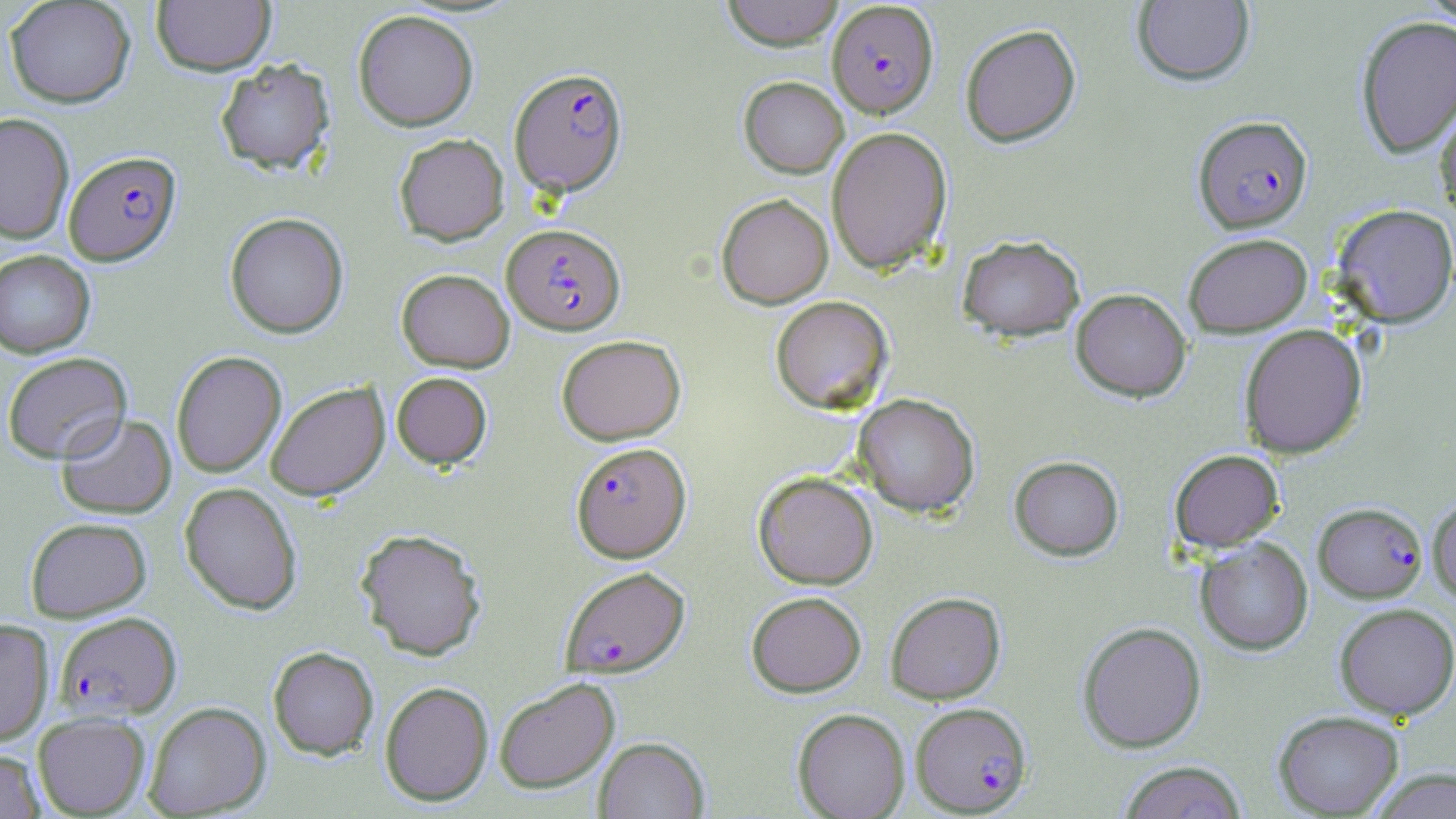

Summary:
  - Coordinate format: approximate bounding boxes as (x1, y1, x2, y2) in pixels
  - Uninfected red blood cell locations: (4, 0, 136, 108), (721, 0, 845, 50), (1418, 0, 1456, 27), (152, 1, 275, 75), (1132, 1, 1255, 86), (353, 9, 479, 131), (1354, 15, 1456, 158), (960, 23, 1081, 147), (215, 58, 335, 175), (738, 76, 849, 178), (1436, 96, 1456, 220), (0, 111, 74, 244), (826, 126, 952, 274), (394, 133, 509, 245), (716, 193, 833, 309), (1332, 203, 1456, 327), (224, 212, 349, 338), (1183, 232, 1313, 338), (957, 234, 1085, 341), (0, 250, 95, 358), (396, 268, 515, 372), (1071, 288, 1192, 402), (770, 295, 893, 413), (1239, 324, 1367, 459), (556, 334, 686, 445), (2, 351, 132, 464), (171, 351, 286, 477), (391, 372, 493, 469), (265, 381, 389, 501), (853, 393, 980, 517), (56, 413, 176, 519), (1170, 449, 1284, 552), (1009, 455, 1124, 560), (753, 471, 878, 589), (180, 482, 302, 615), (1427, 493, 1456, 604), (25, 517, 151, 621), (355, 528, 487, 661), (1195, 538, 1313, 655), (746, 591, 866, 697), (885, 591, 1006, 704), (1334, 602, 1456, 721), (0, 619, 54, 744), (1077, 621, 1206, 752), (268, 646, 379, 760), (494, 677, 620, 793), (379, 681, 493, 806), (143, 701, 271, 818), (792, 708, 910, 819), (1272, 710, 1405, 817), (32, 712, 150, 817), (594, 736, 709, 818), (0, 749, 45, 818), (1117, 761, 1248, 819), (1367, 767, 1456, 818)
  - Plasmodium falciparum-infected red blood cell locations: (827, 1, 939, 118), (509, 67, 628, 196), (1193, 115, 1312, 233), (64, 150, 181, 266), (502, 223, 624, 335), (571, 441, 691, 562), (1313, 502, 1428, 602), (559, 565, 690, 677), (55, 611, 182, 720), (909, 705, 1031, 819)
  - Slide-level diagnosis: Plasmodium falciparum
  - Image size: 1456×819 pixels
  - Preparation: thin blood film
  - Field of view: one of a larger specimen
  - Magnification: 1000x
  - Stain: May-Grünwald-Giemsa
  - Modality: optical microscopy